Report the malaria status of this cell.
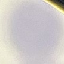

It is uninfected.

capture = smartphone camera at the microscope eyepiece
stain = Giemsa
preparation = thin blood film
image type = cell patch, automatically extracted from a larger field of view and resized to 64 × 64 pixels